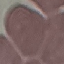
Summary:
  - Result: no malaria parasites seen
  - Stain: Giemsa
  - Image type: automatically extracted cell patch, resized to 64 × 64 pixels
  - Capture: smartphone through the microscope eyepiece
  - Preparation: thin blood smear